Outline each blood parasite and name the species.
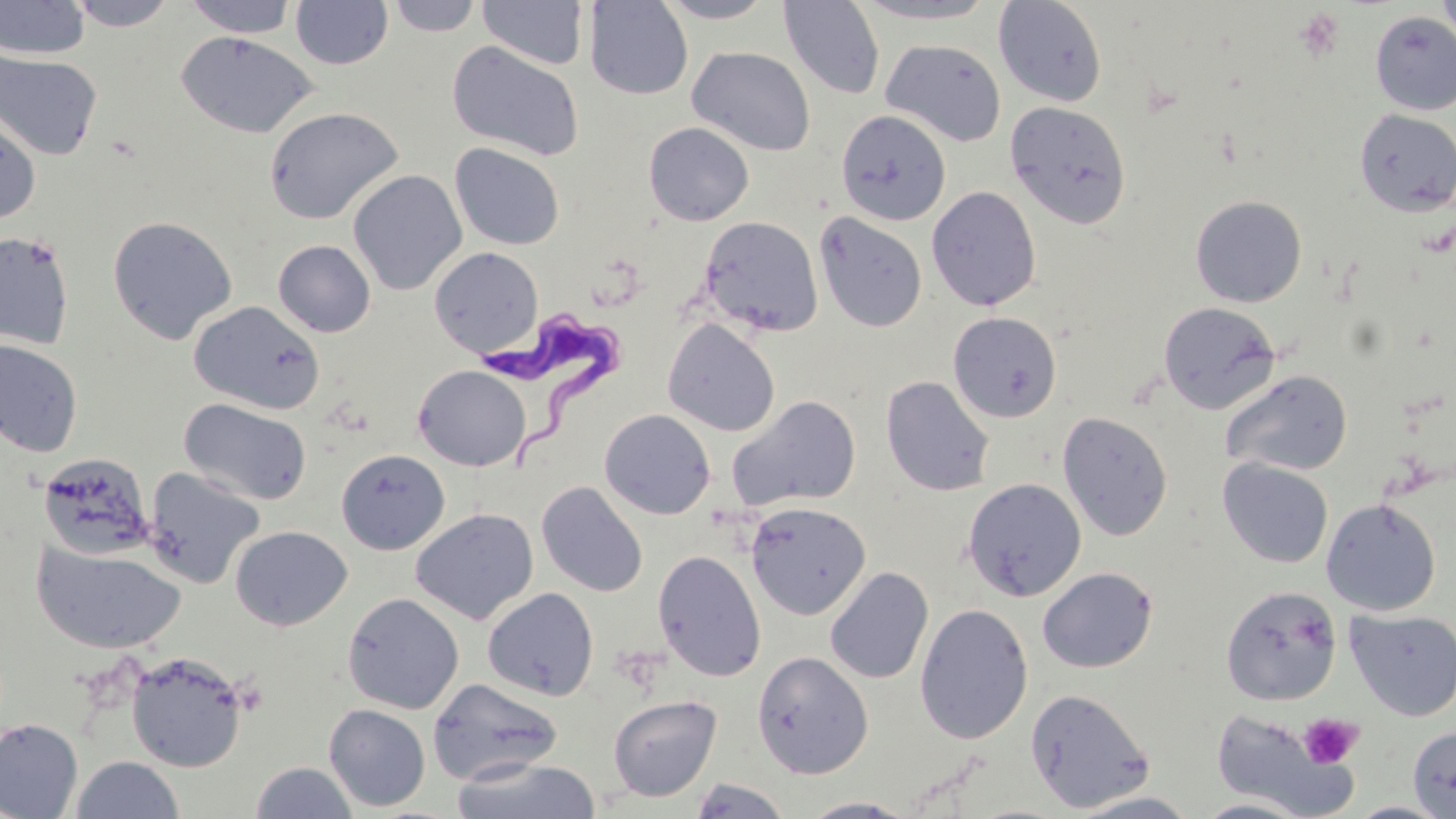
Approximate bounding boxes as named x1/y1/x2/y2 corners in pixels.
Trypanosoma brucei: (x1=481, y1=305, x2=630, y2=477).
No Plasmodium falciparum, Plasmodium ovale, Plasmodium malariae, Plasmodium vivax, or Babesia divergens observed.

Summary:
  - Uninfected red blood cell locations: (x1=1, y1=0, x2=90, y2=60), (x1=66, y1=0, x2=178, y2=31), (x1=184, y1=0, x2=298, y2=37), (x1=291, y1=0, x2=393, y2=69), (x1=387, y1=0, x2=483, y2=36), (x1=583, y1=0, x2=694, y2=100), (x1=656, y1=0, x2=776, y2=23), (x1=778, y1=0, x2=886, y2=100), (x1=854, y1=0, x2=1002, y2=24), (x1=993, y1=0, x2=1109, y2=107), (x1=1437, y1=0, x2=1456, y2=53), (x1=478, y1=1, x2=589, y2=69), (x1=1370, y1=10, x2=1456, y2=116), (x1=176, y1=31, x2=319, y2=139), (x1=881, y1=39, x2=1006, y2=147), (x1=447, y1=41, x2=584, y2=161), (x1=687, y1=46, x2=815, y2=156), (x1=0, y1=51, x2=103, y2=160), (x1=1005, y1=101, x2=1133, y2=230), (x1=263, y1=106, x2=404, y2=225), (x1=1354, y1=109, x2=1456, y2=216), (x1=836, y1=110, x2=951, y2=225), (x1=0, y1=111, x2=41, y2=226), (x1=643, y1=122, x2=754, y2=226), (x1=450, y1=143, x2=565, y2=250), (x1=348, y1=169, x2=467, y2=295), (x1=927, y1=186, x2=1042, y2=311), (x1=1190, y1=195, x2=1307, y2=307), (x1=814, y1=212, x2=927, y2=333), (x1=108, y1=215, x2=238, y2=344), (x1=699, y1=215, x2=824, y2=336), (x1=0, y1=231, x2=75, y2=350), (x1=273, y1=239, x2=375, y2=337), (x1=429, y1=246, x2=543, y2=357), (x1=189, y1=300, x2=325, y2=415), (x1=1158, y1=301, x2=1281, y2=414), (x1=948, y1=311, x2=1063, y2=423), (x1=663, y1=318, x2=780, y2=437), (x1=0, y1=339, x2=82, y2=457), (x1=413, y1=365, x2=532, y2=471), (x1=1221, y1=369, x2=1354, y2=477), (x1=881, y1=376, x2=995, y2=497), (x1=726, y1=395, x2=862, y2=512), (x1=179, y1=397, x2=312, y2=506), (x1=599, y1=408, x2=716, y2=519), (x1=1057, y1=411, x2=1173, y2=541), (x1=336, y1=449, x2=450, y2=555), (x1=38, y1=452, x2=155, y2=559), (x1=1218, y1=459, x2=1334, y2=568), (x1=143, y1=466, x2=266, y2=589), (x1=962, y1=478, x2=1087, y2=602), (x1=536, y1=481, x2=648, y2=597), (x1=1321, y1=498, x2=1441, y2=615), (x1=745, y1=502, x2=871, y2=620), (x1=411, y1=507, x2=539, y2=625), (x1=230, y1=525, x2=353, y2=631), (x1=31, y1=540, x2=187, y2=655), (x1=652, y1=549, x2=766, y2=681), (x1=825, y1=566, x2=934, y2=684), (x1=1037, y1=566, x2=1158, y2=673), (x1=1221, y1=585, x2=1342, y2=705), (x1=482, y1=587, x2=600, y2=701), (x1=342, y1=592, x2=465, y2=714), (x1=914, y1=603, x2=1033, y2=744), (x1=1345, y1=608, x2=1456, y2=721), (x1=125, y1=651, x2=247, y2=772), (x1=751, y1=651, x2=873, y2=779), (x1=427, y1=678, x2=564, y2=786), (x1=1024, y1=687, x2=1156, y2=812), (x1=607, y1=694, x2=722, y2=802), (x1=324, y1=704, x2=431, y2=811), (x1=1209, y1=709, x2=1361, y2=818), (x1=0, y1=718, x2=83, y2=819), (x1=1408, y1=725, x2=1456, y2=818), (x1=71, y1=755, x2=185, y2=818), (x1=451, y1=756, x2=603, y2=819), (x1=250, y1=761, x2=359, y2=818), (x1=685, y1=777, x2=793, y2=818), (x1=1066, y1=790, x2=1203, y2=818), (x1=799, y1=796, x2=922, y2=818), (x1=1191, y1=797, x2=1312, y2=818), (x1=1343, y1=801, x2=1453, y2=819)
  - Platelet locations: (x1=1294, y1=8, x2=1346, y2=61), (x1=1299, y1=713, x2=1363, y2=769)
  - Slide-level diagnosis: Trypanosoma brucei
  - Field of view: single
  - Preparation: thin blood smear
  - Modality: light microscopy
  - Image size: 1456×819 pixels
  - Magnification: 1000x
  - Stain: May-Grünwald-Giemsa